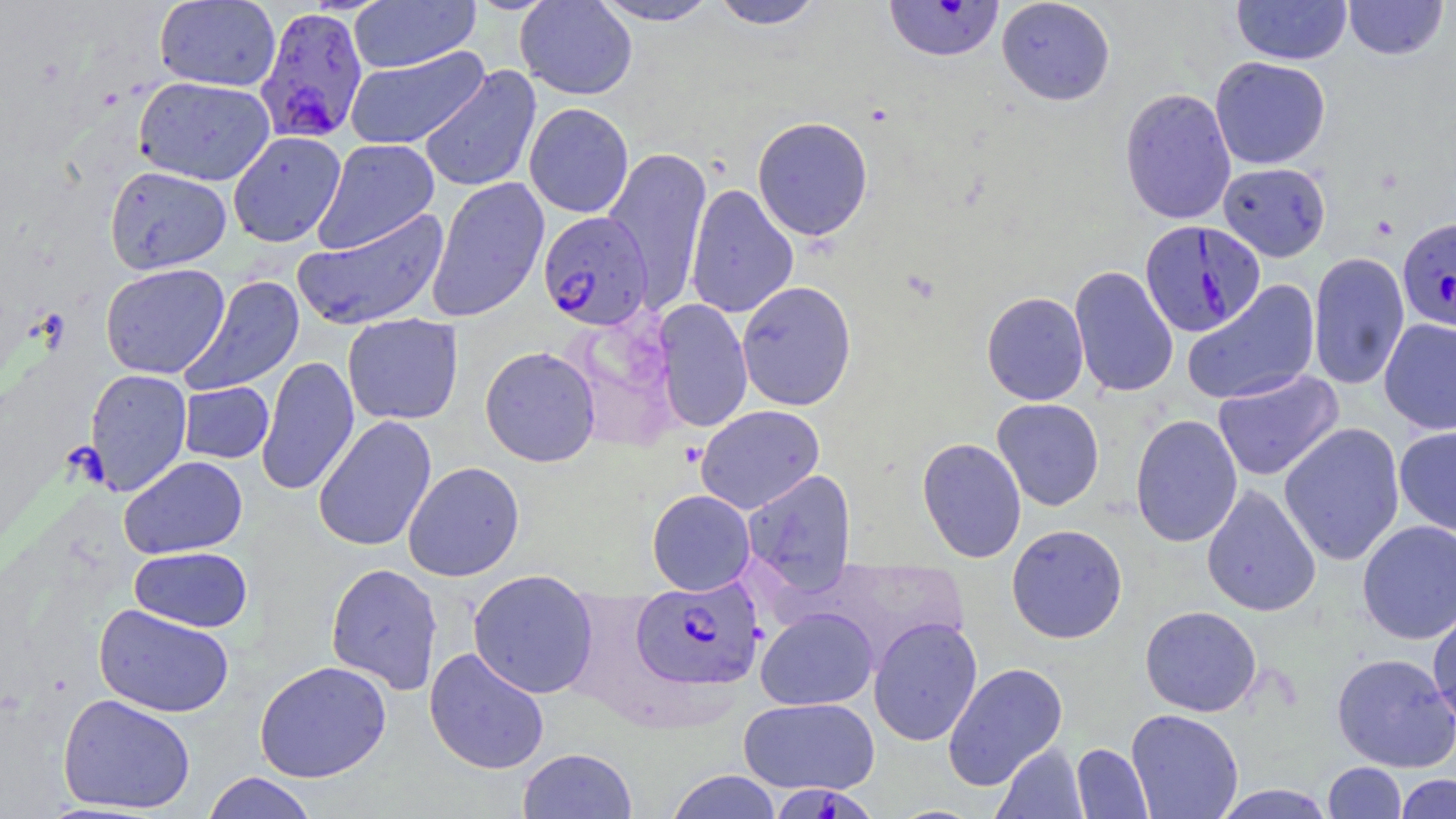 Approximate bounding boxes as (x1,y1)-(x2,y2) corner pairs in pixels. Uninfected red blood cell locations: (515,0)-(637,100), (592,0)-(721,25), (709,0)-(825,29), (996,0)-(1115,105), (1231,0)-(1352,65), (1343,0)-(1448,61), (154,1)-(280,91), (349,1)-(481,72), (344,47)-(490,149), (1210,56)-(1331,170), (419,66)-(542,193), (133,76)-(275,186), (1119,87)-(1236,225), (524,102)-(634,218), (752,116)-(873,241), (227,131)-(346,247), (312,139)-(440,253), (602,146)-(712,312), (1218,162)-(1332,261), (104,165)-(232,274), (426,177)-(549,322), (685,183)-(799,319), (292,208)-(450,331), (1308,251)-(1409,392), (100,263)-(230,379), (1069,265)-(1179,398), (179,275)-(305,397), (736,280)-(857,411), (1181,280)-(1321,406), (982,291)-(1089,405), (653,300)-(753,433), (566,312)-(682,451), (342,313)-(463,425), (1379,318)-(1456,435), (479,346)-(601,467), (256,355)-(359,496), (84,368)-(193,495), (1212,369)-(1343,481), (179,382)-(274,464), (991,398)-(1105,511), (695,405)-(825,514), (1130,414)-(1243,548), (313,415)-(437,552), (1278,423)-(1405,566), (1394,427)-(1456,536), (916,437)-(1027,563), (119,455)-(248,559), (403,461)-(525,581), (742,469)-(857,595), (1201,483)-(1321,618), (647,489)-(756,596), (1357,520)-(1456,644), (1006,523)-(1128,644), (129,546)-(253,632), (325,562)-(444,695), (468,569)-(599,699), (1427,602)-(1456,732), (94,603)-(235,718), (1140,605)-(1262,717), (756,607)-(878,710), (868,616)-(983,747), (424,647)-(550,775), (1332,653)-(1456,773), (254,661)-(392,783), (943,662)-(1068,790), (57,693)-(196,814), (738,697)-(880,795), (1126,708)-(1244,819), (992,743)-(1087,819), (1071,743)-(1154,818), (517,747)-(638,818), (1322,762)-(1406,818), (666,769)-(782,819), (201,772)-(319,819), (1395,773)-(1455,818), (1212,784)-(1336,818). Plasmodium falciparum-infected red blood cell locations: (884,1)-(1004,62), (254,5)-(369,145), (538,211)-(655,331), (1398,217)-(1456,332), (1139,220)-(1265,337), (631,577)-(764,690), (772,785)-(877,819). Slide-level diagnosis: Plasmodium falciparum. One field of a larger specimen. May-Grünwald-Giemsa stain. Light microscopy. 1000x magnification. Image is 1456×819 pixels. Thin blood film.